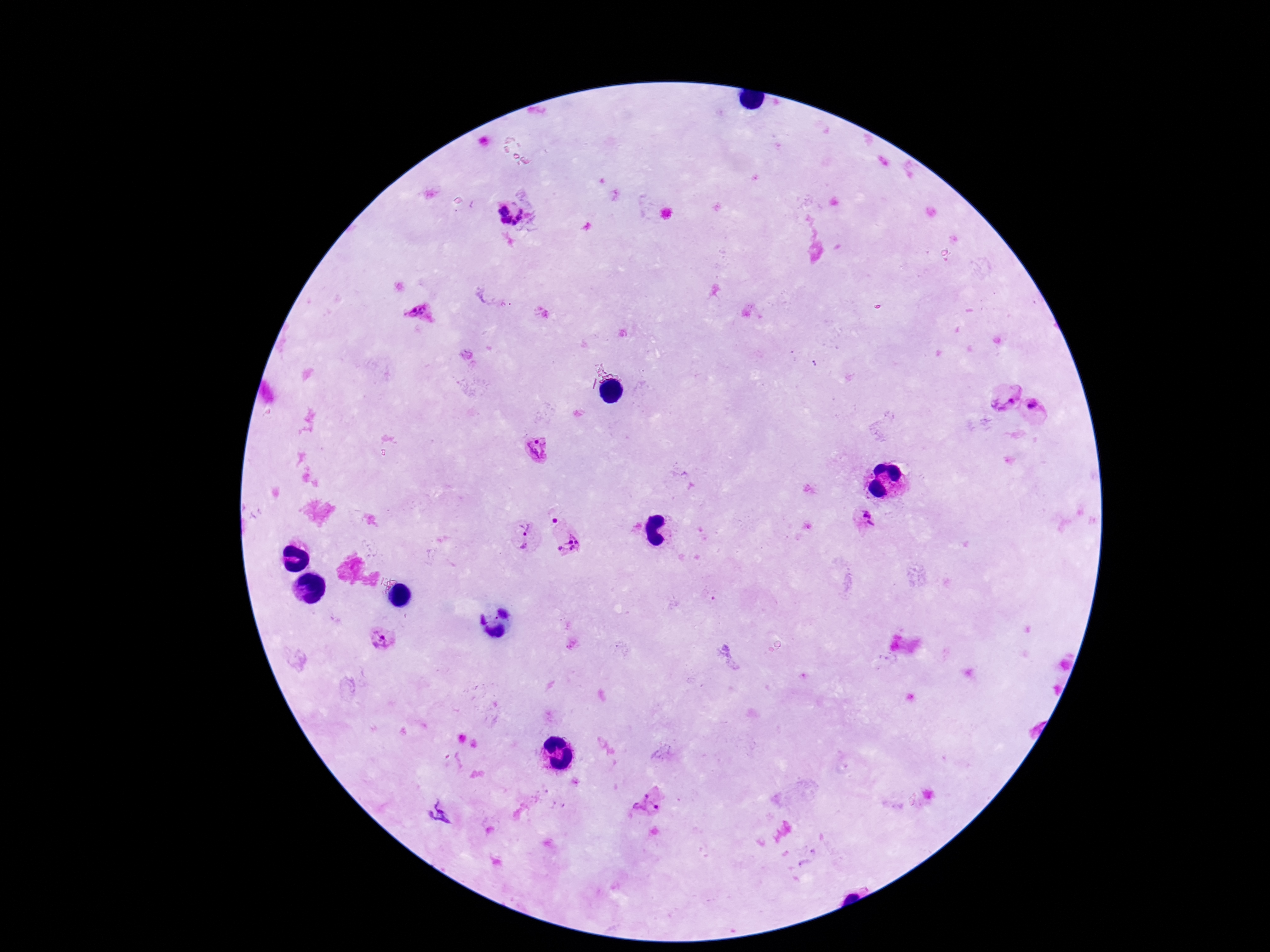

capture = smartphone camera through the microscope eyepiece
stain = Giemsa
field of view = one from this slide
image size = 1270×952 pixels
patient malaria status = infected
preparation = thick peripheral-blood smear
Plasmodium parasite locations = approximate centers as (x, y) in pixels: (507, 214), (420, 314), (1008, 395), (1038, 408), (538, 451), (553, 518), (867, 518), (525, 528), (570, 544), (523, 546), (383, 638), (646, 805)
magnification = 100x